State the preparation type.
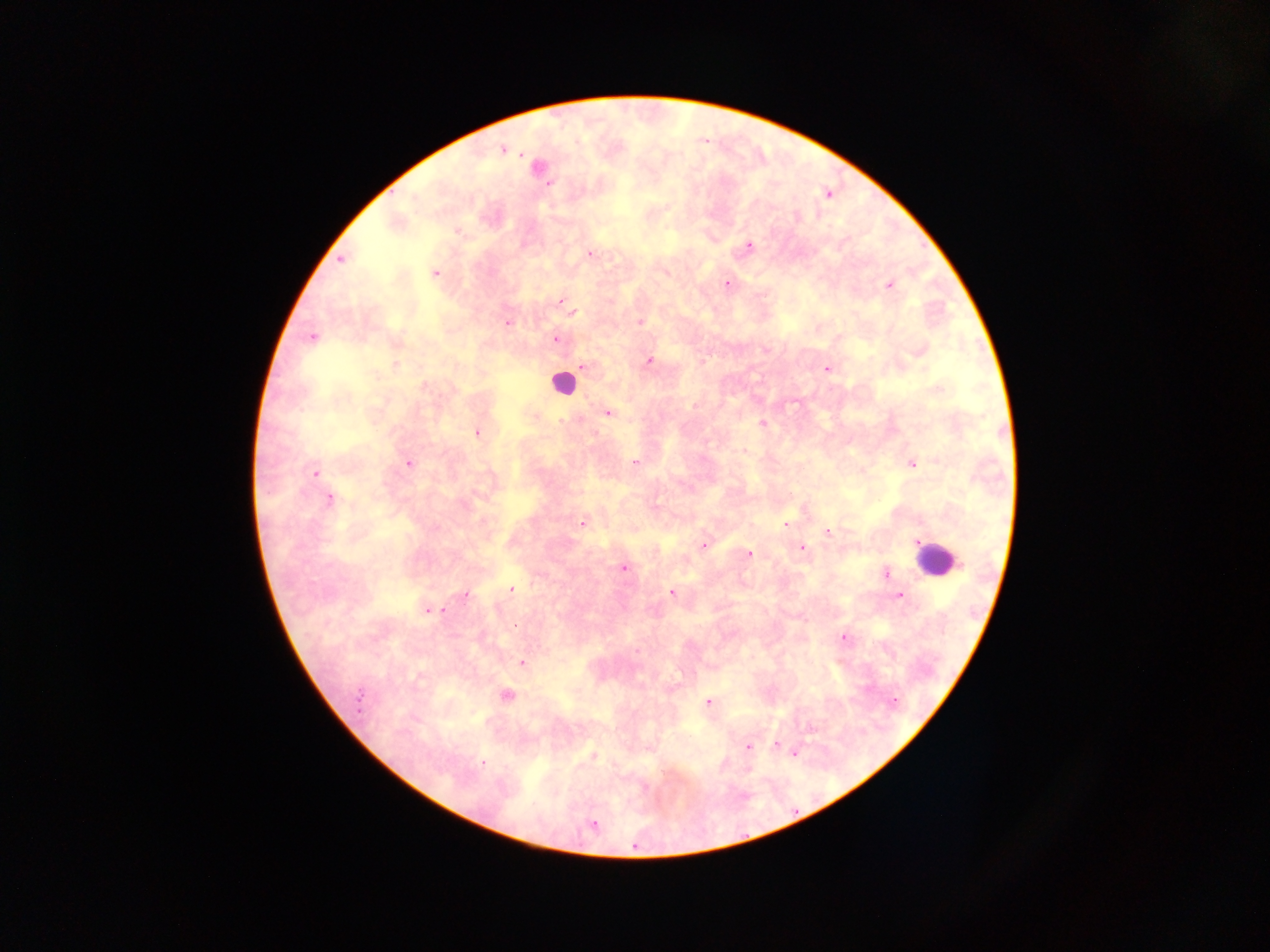

Thick blood smear.

capture = mobile-phone photograph through a microscope
country = Ghana
Plasmodium parasite locations = approximate centers as x y in pixels: 503 149; 537 167; 828 194; 395 222; 457 232; 747 246; 590 254; 342 259; 435 272; 727 283; 888 284; 560 301; 571 312; 639 322; 507 323; 312 336; 555 339; 395 342; 919 349; 648 361; 585 366; 826 368; 607 412; 533 415; 762 423; 477 431; 745 450; 911 462; 409 463; 634 463; 861 471; 314 472; 328 498; 583 522; 786 523; 827 533; 917 543; 704 544; 801 547; 748 553; 623 567; 885 573; 511 589; 672 593; 463 594; 899 595; 427 611; 844 638; 520 662; 504 694; 893 701; 708 702; 775 744; 749 746; 793 752; 592 756; 482 763; 592 824
leukocyte locations = approximate centers as x y in pixels: 562 383; 937 560
field of view = single
image size = 1270×952 pixels